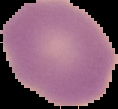
image_type: segmented cell region with the area outside set to black
image_size: 118×109 pixels
preparation: thin blood film
result: no malaria parasites seen